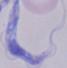
1000x magnification. Photomicrograph. A trypanosome is seen.